Locate and identify every blood parasite.
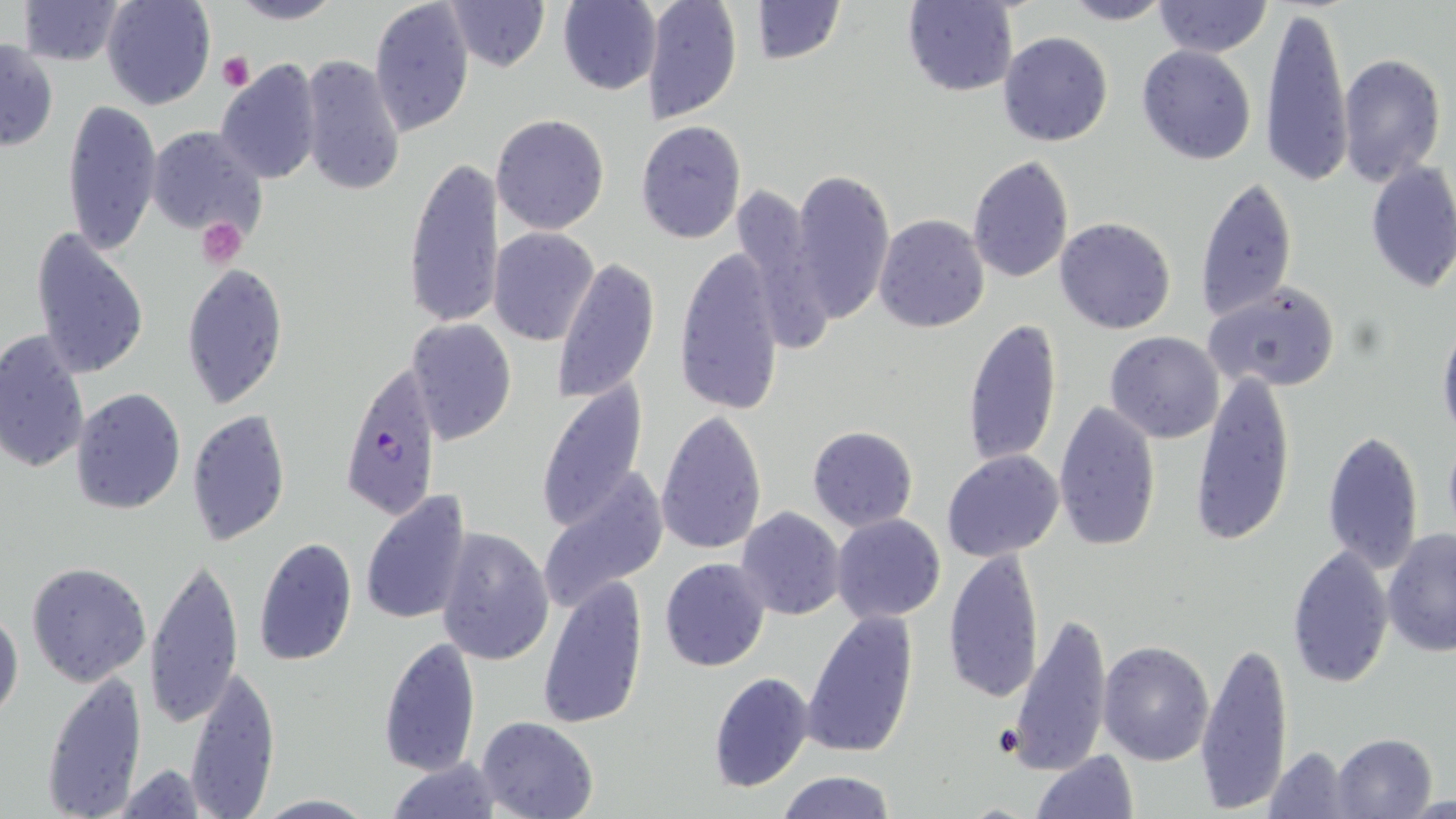
Approximate bounding boxes as [x1, y1, x2, y2] in pixels.
Plasmodium falciparum-infected red blood cells: [337, 361, 444, 520].
No Plasmodium ovale, Plasmodium malariae, Plasmodium vivax, Babesia divergens, or Trypanosoma brucei observed.

Uninfected red blood cell locations: [15, 0, 128, 66], [101, 0, 215, 109], [225, 0, 345, 25], [369, 0, 476, 140], [443, 0, 550, 72], [640, 0, 744, 124], [747, 0, 846, 64], [1152, 0, 1271, 57], [903, 1, 1017, 97], [1059, 1, 1173, 25], [557, 2, 661, 95], [1262, 3, 1353, 187], [998, 31, 1113, 147], [1, 38, 58, 153], [1138, 45, 1257, 165], [1338, 53, 1445, 187], [299, 54, 406, 196], [215, 58, 325, 185], [61, 97, 163, 257], [490, 113, 610, 236], [635, 120, 747, 245], [145, 125, 269, 241], [967, 154, 1076, 285], [402, 156, 506, 332], [1364, 160, 1456, 297], [790, 169, 895, 324], [1194, 176, 1298, 323], [729, 182, 833, 356], [873, 214, 990, 333], [1053, 217, 1177, 335], [31, 227, 149, 381], [488, 227, 600, 346], [672, 245, 787, 419], [553, 257, 661, 404], [181, 261, 289, 409], [1204, 283, 1339, 393], [961, 317, 1063, 469], [406, 318, 516, 443], [1437, 321, 1456, 443], [0, 329, 90, 477], [1104, 332, 1225, 443], [1190, 369, 1299, 547], [534, 382, 650, 533], [70, 387, 186, 514], [1052, 399, 1162, 552], [188, 408, 292, 547], [655, 409, 768, 556], [806, 425, 918, 532], [1321, 430, 1424, 578], [942, 450, 1065, 563], [536, 473, 667, 613], [360, 489, 472, 624], [736, 506, 845, 620], [830, 513, 946, 623], [434, 527, 555, 666], [1382, 529, 1455, 657], [252, 535, 358, 668], [1286, 545, 1394, 688], [942, 546, 1042, 705], [144, 556, 246, 729], [660, 557, 771, 672], [25, 560, 153, 686], [537, 573, 650, 730], [0, 605, 24, 724], [1009, 610, 1113, 778], [802, 612, 919, 756], [378, 637, 482, 776], [1098, 640, 1216, 766], [1196, 640, 1295, 816], [184, 664, 280, 818], [40, 671, 148, 815], [706, 672, 813, 792], [476, 716, 599, 819], [1332, 733, 1437, 818], [1260, 746, 1357, 818], [1030, 750, 1140, 819], [386, 756, 504, 817], [110, 763, 214, 818], [777, 769, 896, 819], [253, 794, 380, 817], [1406, 795, 1456, 817]. Platelet locations: [217, 52, 254, 90], [195, 218, 249, 267]. Slide-level diagnosis: Plasmodium falciparum. Image is 1456×819 pixels. Optical microscopy. May-Grünwald-Giemsa-stained preparation. Single field of view. Thin blood smear. 1000x magnification.